Locate every Plasmodium falciparum-infected red blood cell.
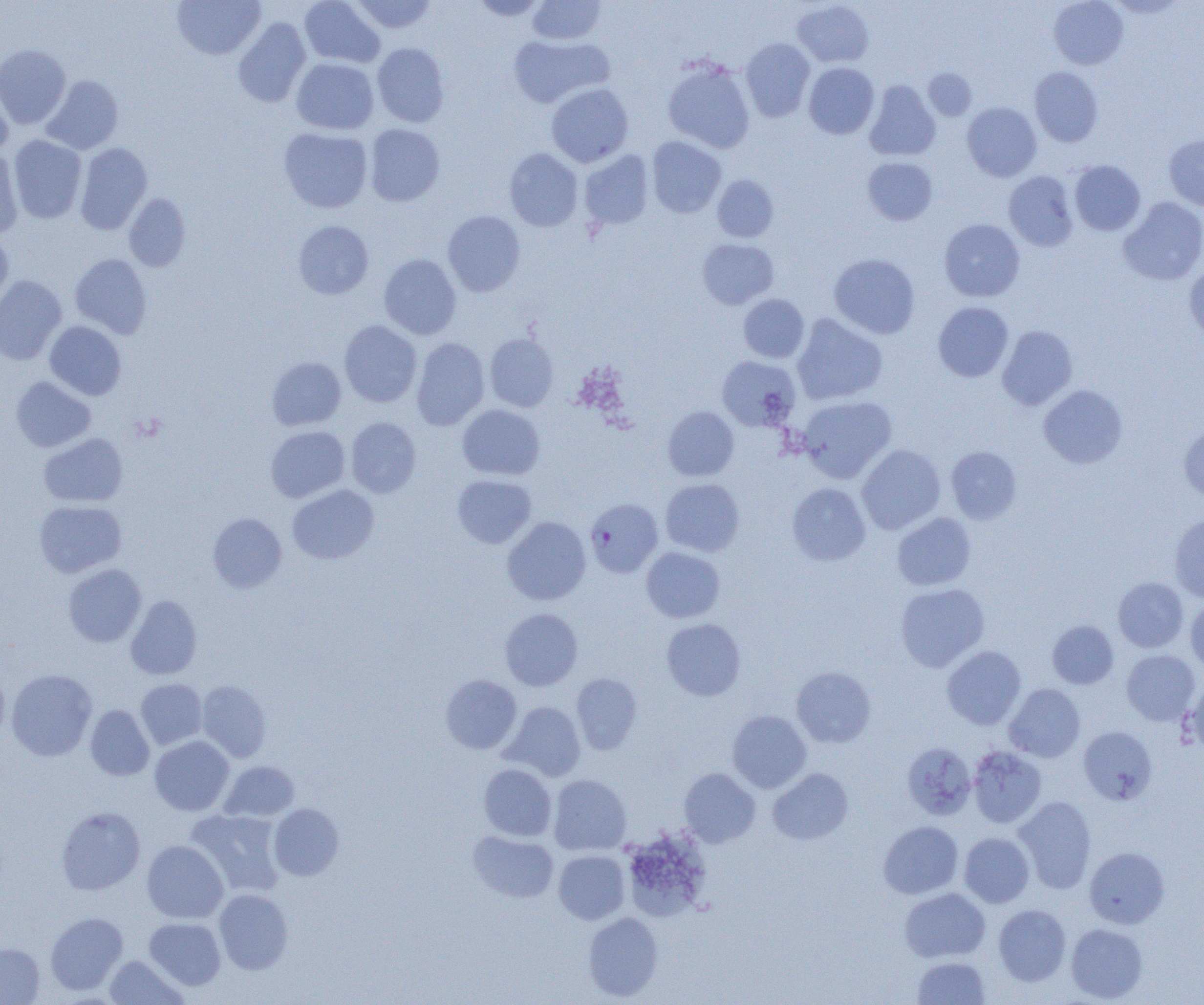
Approximate bounding boxes as [x1, y1, x2, y2] in pixels.
Plasmodium falciparum-infected red blood cells: [585, 498, 663, 577].

Summary:
  - Uninfected red blood cell locations: [172, 0, 266, 60], [299, 0, 385, 67], [350, 0, 437, 34], [470, 0, 549, 21], [527, 0, 606, 45], [1048, 0, 1128, 69], [1106, 0, 1186, 19], [792, 1, 874, 68], [232, 17, 311, 108], [508, 34, 613, 108], [740, 38, 815, 121], [372, 43, 449, 127], [0, 44, 71, 129], [291, 58, 379, 134], [662, 58, 756, 153], [803, 63, 879, 139], [1029, 67, 1103, 147], [923, 68, 977, 120], [0, 74, 14, 157], [40, 75, 124, 154], [864, 80, 941, 161], [546, 83, 633, 167], [962, 102, 1042, 181], [364, 124, 445, 207], [278, 127, 373, 213], [8, 135, 86, 223], [1164, 135, 1204, 210], [646, 136, 726, 218], [75, 142, 152, 234], [504, 148, 583, 231], [0, 149, 24, 239], [579, 151, 654, 230], [862, 156, 938, 225], [1069, 160, 1145, 236], [1003, 171, 1079, 252], [712, 174, 779, 242], [124, 193, 191, 271], [1118, 197, 1204, 285], [443, 210, 525, 296], [939, 219, 1025, 302], [293, 220, 374, 299], [0, 234, 13, 308], [697, 238, 779, 309], [70, 253, 152, 338], [379, 253, 462, 340], [829, 253, 920, 338], [1184, 263, 1204, 344], [0, 275, 66, 364], [738, 294, 810, 363], [933, 302, 1014, 382], [792, 313, 887, 405], [339, 320, 422, 407], [45, 321, 126, 400], [997, 325, 1078, 410], [484, 333, 559, 412], [411, 338, 490, 430], [716, 355, 801, 432], [266, 357, 346, 430], [11, 376, 96, 452], [1038, 384, 1127, 469], [798, 396, 896, 482], [457, 404, 545, 480], [663, 406, 739, 481], [346, 417, 421, 498], [1178, 423, 1204, 502], [265, 426, 350, 502], [39, 433, 128, 507], [856, 444, 946, 534], [946, 446, 1022, 524], [452, 474, 537, 548], [660, 478, 745, 556], [786, 483, 871, 567], [287, 484, 379, 564], [34, 500, 127, 577], [208, 513, 287, 593], [892, 513, 976, 591], [1168, 514, 1204, 602], [502, 516, 591, 605], [641, 546, 725, 623], [63, 563, 146, 647], [1113, 577, 1189, 652], [895, 583, 989, 671], [126, 595, 202, 680], [1186, 598, 1204, 676], [500, 608, 583, 691], [661, 618, 746, 700], [1047, 620, 1119, 689], [942, 646, 1026, 729], [1121, 649, 1200, 726], [791, 665, 876, 747], [0, 666, 10, 745], [6, 669, 97, 761], [571, 673, 643, 754], [440, 675, 521, 754], [135, 679, 207, 749], [1183, 679, 1204, 756], [197, 680, 272, 762], [1004, 683, 1085, 762], [502, 701, 585, 780], [85, 705, 155, 780], [727, 710, 811, 793], [1078, 726, 1157, 805], [149, 736, 234, 815], [902, 742, 977, 820], [968, 746, 1047, 828], [219, 761, 299, 822], [478, 764, 556, 841], [679, 768, 761, 847], [767, 768, 853, 845], [548, 774, 631, 854], [1014, 796, 1097, 893], [268, 803, 344, 881], [56, 806, 145, 895], [186, 809, 285, 897], [878, 821, 963, 899], [621, 829, 712, 921], [468, 831, 559, 903], [959, 832, 1035, 907], [142, 841, 228, 923], [1084, 846, 1169, 928], [553, 850, 629, 924], [900, 887, 990, 962], [214, 889, 292, 974], [993, 904, 1071, 986], [45, 912, 128, 995], [582, 913, 663, 1001], [144, 917, 226, 990], [1065, 923, 1148, 1002], [0, 943, 44, 1004], [104, 955, 188, 1004], [912, 957, 991, 1004]
  - Slide-level diagnosis: Plasmodium falciparum
  - Magnification: 1000x
  - Field of view: single
  - Preparation: thin blood film
  - Image size: 1204×1005 pixels
  - Modality: optical microscopy